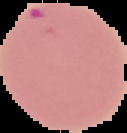

Summary:
  - Malaria status: parasitized
  - Image type: segmented cell region on a black background
  - Preparation: thin blood smear
  - Image size: 127×133 pixels